Point out each Plasmodium parasite.
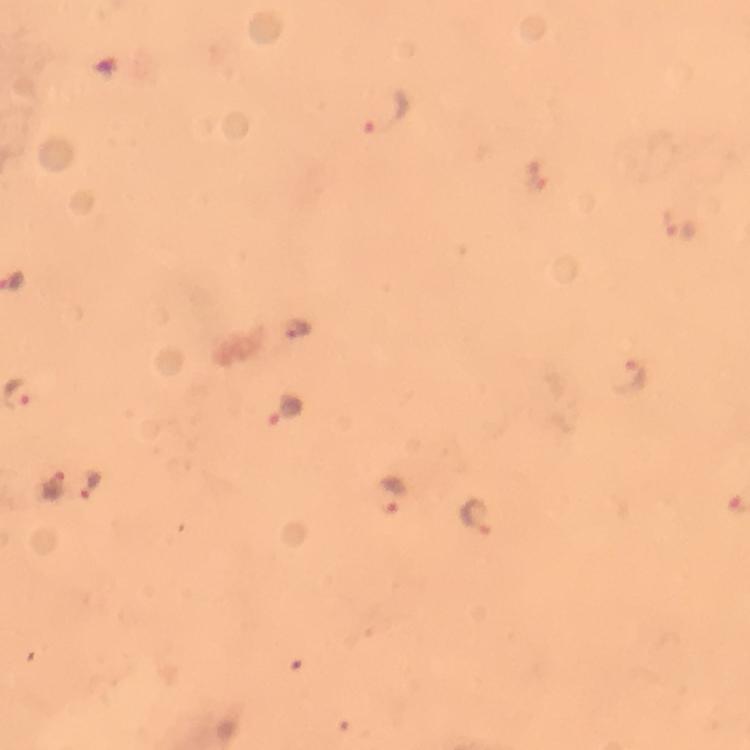

Approximate object centers, in pixels from the top-left corner.
Plasmodium parasites: (x=385, y=109), (x=684, y=226), (x=298, y=328), (x=631, y=380), (x=284, y=410), (x=52, y=485), (x=91, y=488), (x=389, y=496), (x=475, y=515).

Image is 750×750 pixels. 100x magnification. A crop from one field of view. Immersion oil was used. From a diagnostic examination for malaria. Smartphone photograph taken through a microscope. Giemsa stain. Thick blood smear.